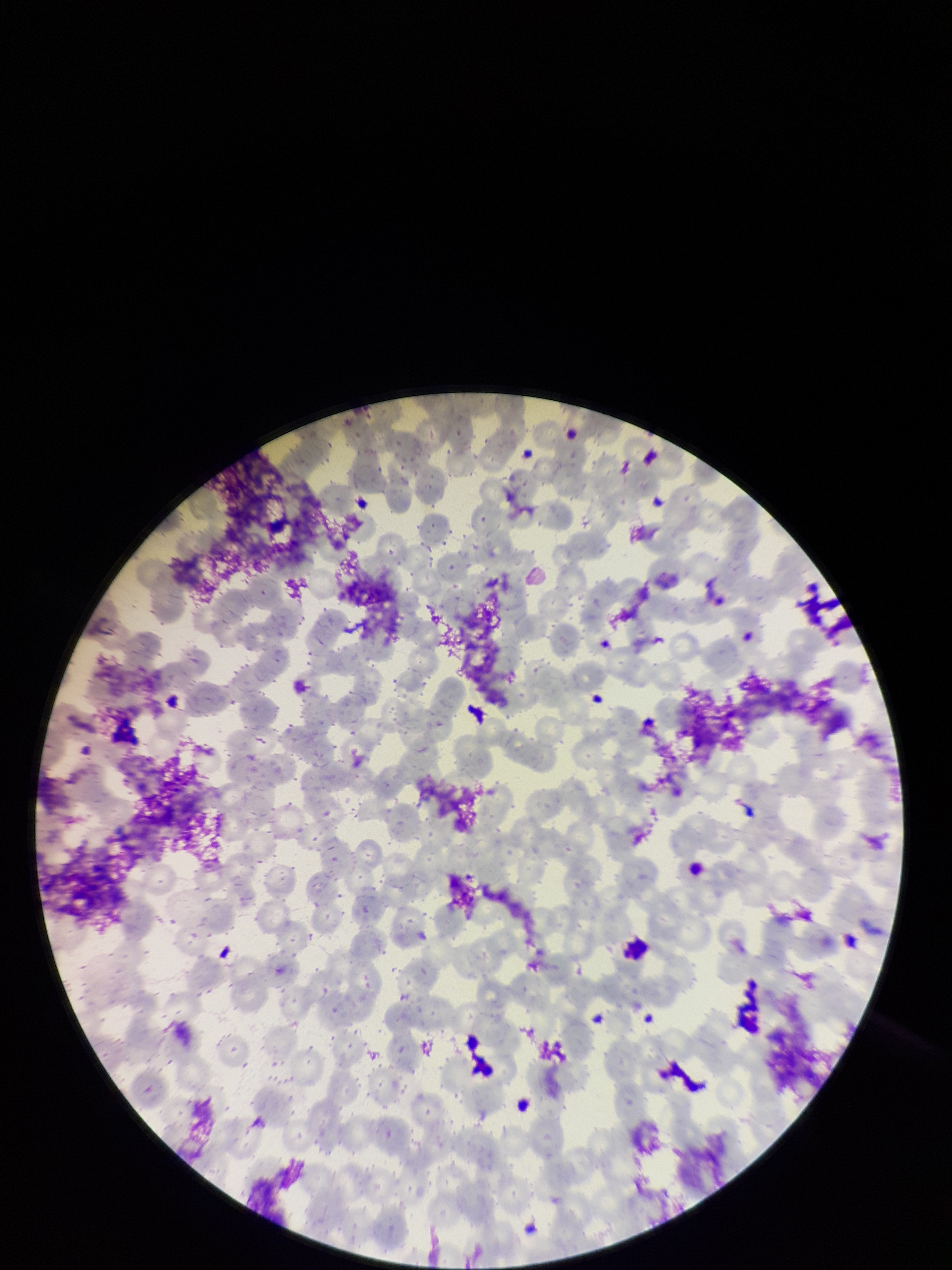

parasitized red blood cells = none seen
capture = smartphone photograph through the microscope eyepiece
parasitized red blood cell count = 0
patient malaria status = negative
field of view = one from this slide
red blood cell count = 287
stain = Giemsa
image size = 952×1270 pixels
preparation = thin blood smear